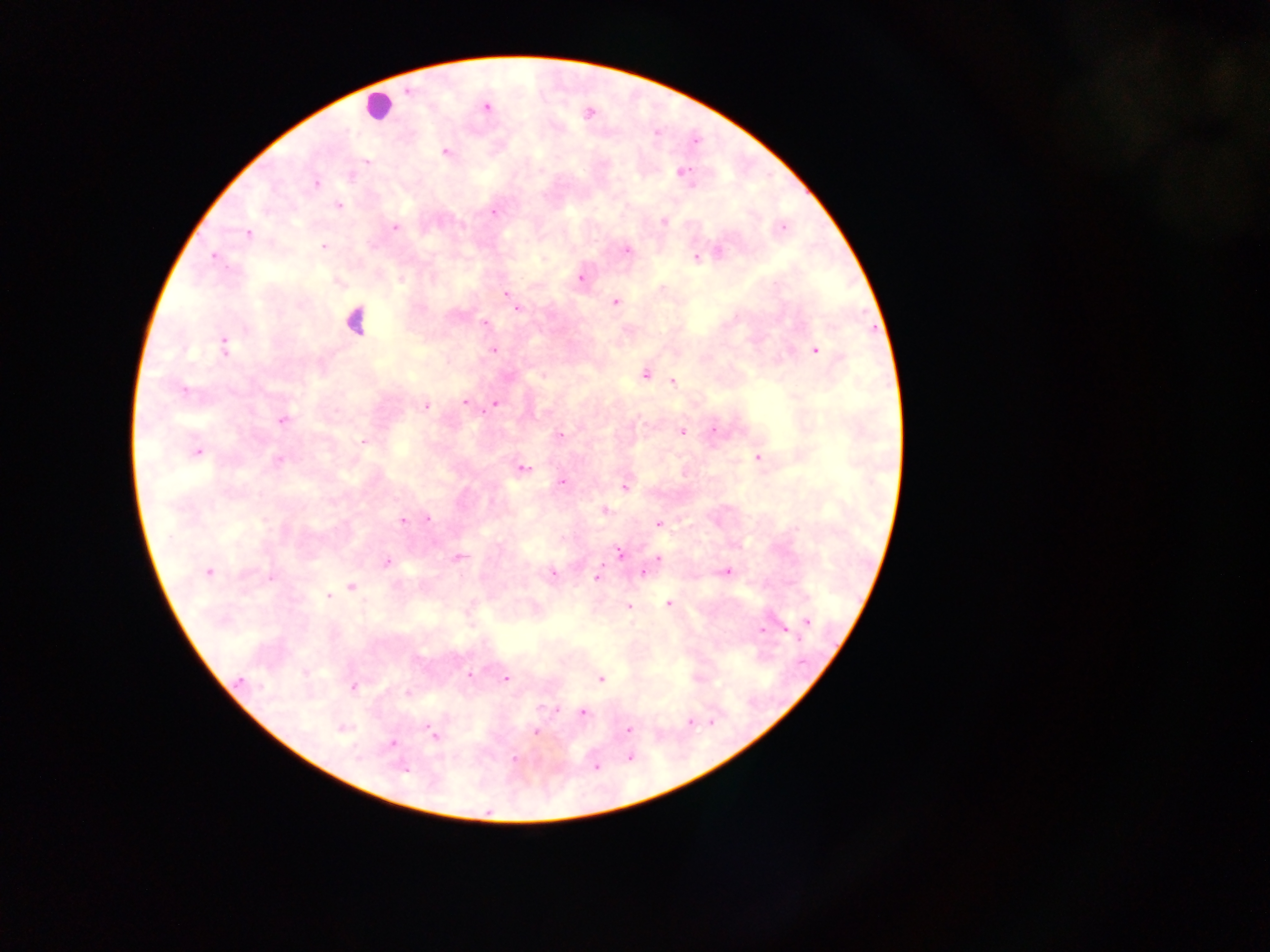

Approximate centers as [x, y] in pixels. Leukocyte locations: [377, 105], [355, 319]. Plasmodium parasite locations: [408, 91], [486, 108], [695, 142], [445, 152], [366, 161], [682, 172], [316, 184], [338, 206], [493, 212], [663, 221], [395, 228], [783, 228], [249, 234], [324, 246], [627, 250], [719, 252], [213, 256], [696, 257], [581, 277], [506, 294], [615, 302], [518, 308], [485, 324], [224, 347], [493, 350], [816, 350], [645, 375], [672, 381], [183, 389], [464, 402], [495, 404], [425, 406], [283, 420], [713, 430], [682, 432], [560, 435], [363, 442], [197, 451], [758, 458], [278, 460], [523, 468], [561, 482], [624, 489], [605, 511], [428, 518], [403, 522], [658, 523], [618, 552], [460, 557], [658, 558], [386, 561], [208, 571], [728, 572], [553, 573], [643, 573], [271, 578], [597, 578], [351, 587], [327, 596], [668, 603], [629, 606], [807, 621], [762, 629], [785, 630], [305, 673], [469, 674], [506, 679], [601, 679], [240, 680], [353, 686], [583, 713], [689, 721], [342, 730], [629, 730], [536, 732], [433, 734], [392, 744], [629, 757], [513, 759], [597, 768], [403, 769]. Thick blood film. Photographed through a microscope with a mobile-phone camera. Image is 1270×952 pixels. Single field of view. Collected in Ghana.